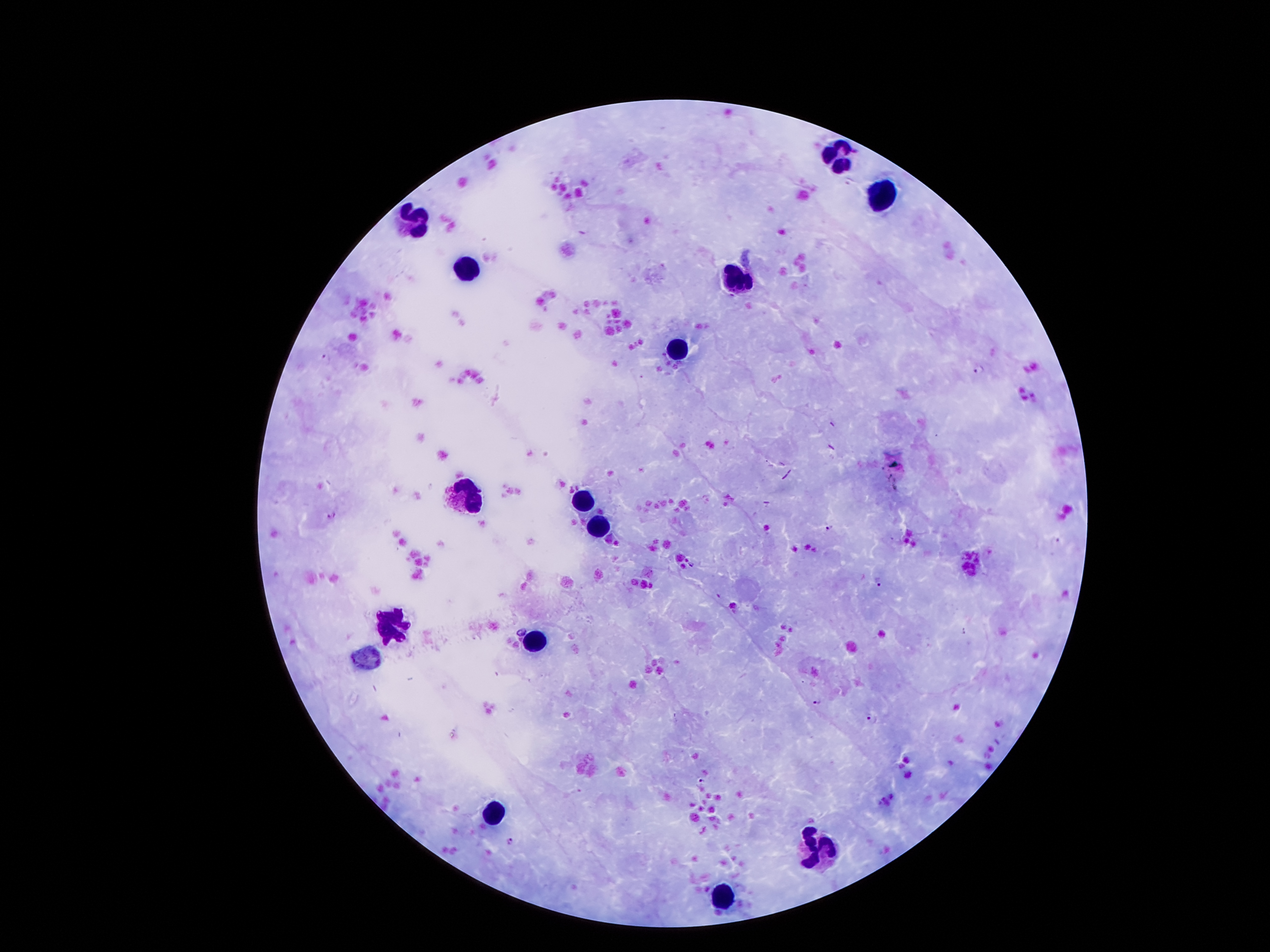
Approximate centers as (x, y) in pixels.
Summary:
  - Leukocyte locations: (837, 153), (877, 193), (409, 220), (467, 271), (739, 277), (678, 351), (466, 492), (582, 501), (599, 529), (393, 624), (535, 640), (490, 812), (821, 852), (722, 897)
  - Malaria parasite locations: (324, 358), (979, 368), (331, 514), (829, 527), (1055, 540), (691, 565), (877, 582), (522, 630), (816, 700), (872, 719), (701, 780), (510, 841)
  - Magnification: 100x
  - Image size: 1270×952 pixels
  - Stain: Giemsa
  - Capture: smartphone camera through the microscope eyepiece
  - Preparation: thick blood smear
  - Patient malaria status: positive for Plasmodium falciparum
  - Field of view: single